Describe the morphology of the red blood cells.
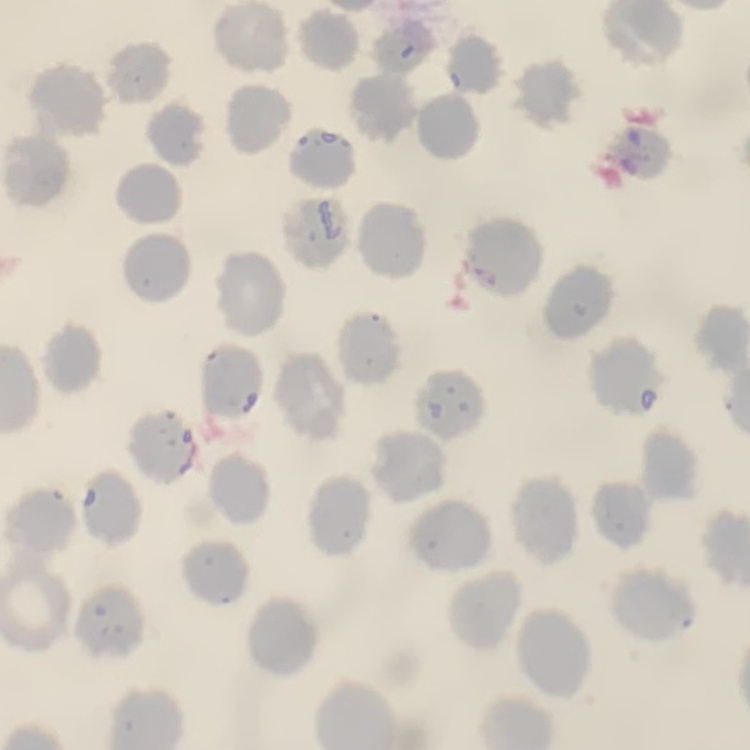

They show no rouleaux formation.

Thin blood smear. Square crop of a larger photomicrograph. Stained with either Field's or Giemsa.